State which cell type is depicted.
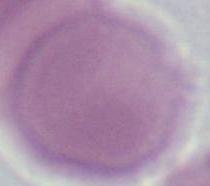

This is an erythrocyte.

Micrograph. Captured at 1000x magnification.